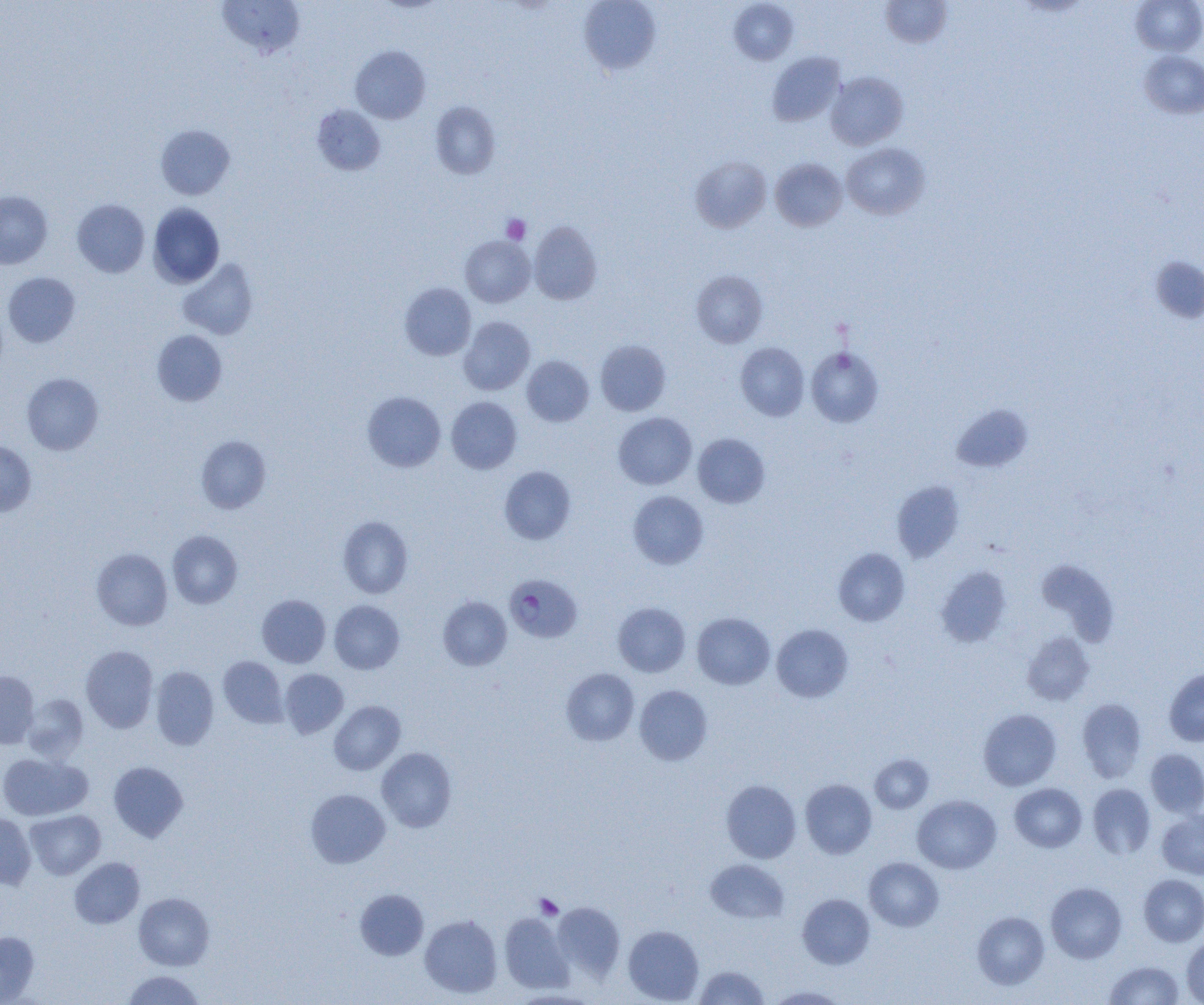
Summary:
  - Coordinate format: approximate bounding boxes as [x1, y1, x2, y2] in pixels
  - Plasmodium falciparum-infected red blood cell locations: [504, 574, 583, 643]
  - Platelet locations (subset): [501, 214, 530, 244], [534, 894, 563, 919]
  - Uninfected red blood cell locations (subset): [217, 0, 305, 58], [578, 0, 661, 75], [881, 0, 952, 48], [1131, 0, 1204, 56], [729, 1, 799, 65], [350, 46, 430, 124], [1139, 50, 1204, 118], [767, 52, 846, 126], [826, 72, 908, 150], [430, 101, 501, 179], [312, 105, 386, 175], [156, 124, 235, 200], [841, 142, 930, 220], [690, 156, 771, 233], [770, 158, 847, 231], [0, 191, 52, 269], [72, 199, 149, 277], [148, 203, 224, 287], [528, 221, 602, 305], [460, 236, 535, 307], [177, 258, 259, 340], [691, 270, 768, 347], [3, 272, 80, 348], [400, 283, 476, 360], [458, 316, 535, 395], [152, 330, 227, 406], [595, 339, 670, 416], [735, 342, 809, 421], [806, 347, 884, 428], [522, 355, 594, 427], [22, 373, 103, 455], [363, 391, 445, 472], [446, 397, 522, 473], [951, 404, 1032, 473], [613, 412, 696, 490], [693, 433, 770, 508], [196, 435, 271, 513], [0, 441, 36, 517], [499, 466, 576, 544], [891, 481, 964, 563], [628, 491, 709, 569], [338, 516, 413, 598], [167, 530, 243, 609], [92, 548, 172, 630], [833, 548, 910, 627], [1035, 558, 1119, 645], [935, 565, 1011, 647], [257, 594, 330, 668], [439, 596, 512, 670], [329, 600, 405, 674], [613, 602, 691, 677], [692, 612, 774, 689], [771, 624, 853, 703], [1022, 632, 1094, 705], [80, 646, 158, 733], [218, 656, 288, 728], [151, 666, 219, 750], [561, 668, 639, 746], [1164, 668, 1204, 747], [279, 669, 349, 738], [0, 671, 39, 748], [634, 685, 712, 765], [22, 694, 89, 762], [1077, 697, 1147, 782], [329, 701, 405, 775], [978, 708, 1061, 790], [377, 747, 456, 832], [1145, 749, 1204, 818], [0, 753, 91, 820], [870, 754, 934, 813], [108, 761, 188, 842], [721, 779, 802, 863], [800, 779, 876, 859], [1009, 783, 1087, 852], [1087, 783, 1156, 859], [306, 789, 390, 868], [912, 795, 1001, 874], [25, 810, 105, 879], [1156, 810, 1204, 880], [0, 813, 36, 889], [70, 857, 145, 928], [864, 857, 944, 932], [705, 859, 789, 923], [1138, 874, 1204, 947], [1046, 882, 1127, 963], [355, 889, 428, 960], [134, 893, 214, 970], [797, 893, 875, 969], [552, 902, 625, 980], [972, 911, 1049, 990], [499, 913, 572, 993], [420, 914, 502, 998], [623, 925, 704, 1004], [0, 932, 39, 1003], [1182, 935, 1204, 1004], [1104, 960, 1184, 1004], [693, 965, 769, 1005], [122, 970, 205, 1004], [767, 986, 847, 1004]
  - Slide-level diagnosis: Plasmodium falciparum
  - Modality: optical microscopy
  - Image size: 1204×1005 pixels
  - Preparation: thin blood smear
  - Field of view: one of a larger specimen
  - Magnification: 1000x